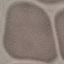

Result: no malaria parasites seen. Photographed with a smartphone camera at the microscope eyepiece. Giemsa-stained preparation. Cell patch, automatically extracted from a larger field of view and resized to 64 × 64 pixels. Thin blood smear.